Point out each Plasmodium parasite.
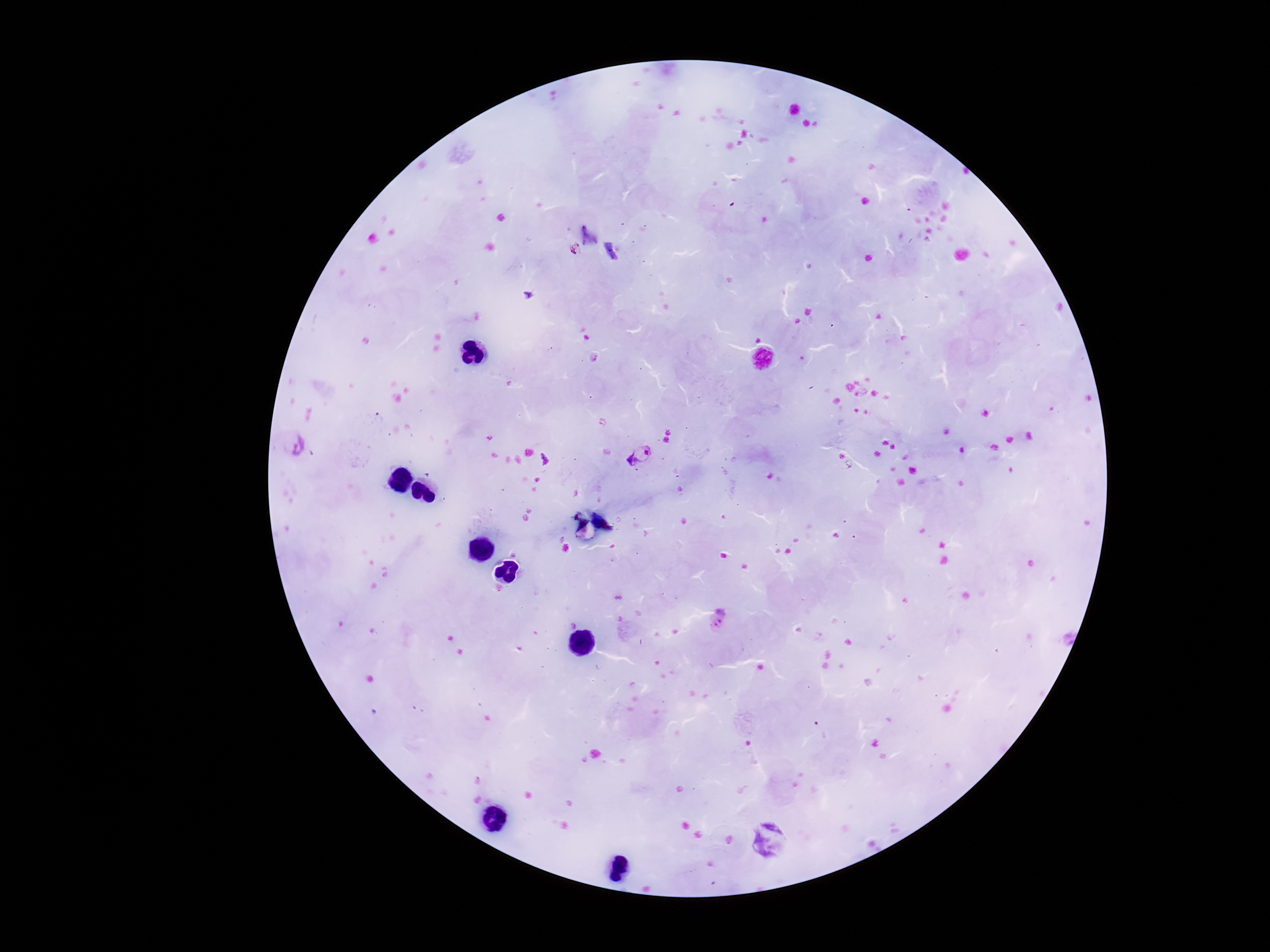

Approximate centers as {x, y} in pixels.
Plasmodium parasites: {573, 250}, {293, 445}, {639, 453}, {544, 459}, {718, 623}.

Giemsa-stained preparation. Photographed through the microscope eyepiece with a smartphone camera. Thick blood smear. Single field of view. Patient malaria status: infected. 100x magnification. Image is 1270×952 pixels.